Assess this cell for malaria.
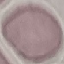
Uninfected.

Giemsa stain. Photographed with a smartphone camera at the microscope eyepiece. Automatically extracted cell patch, resized to 64 × 64 pixels. Thin blood film.